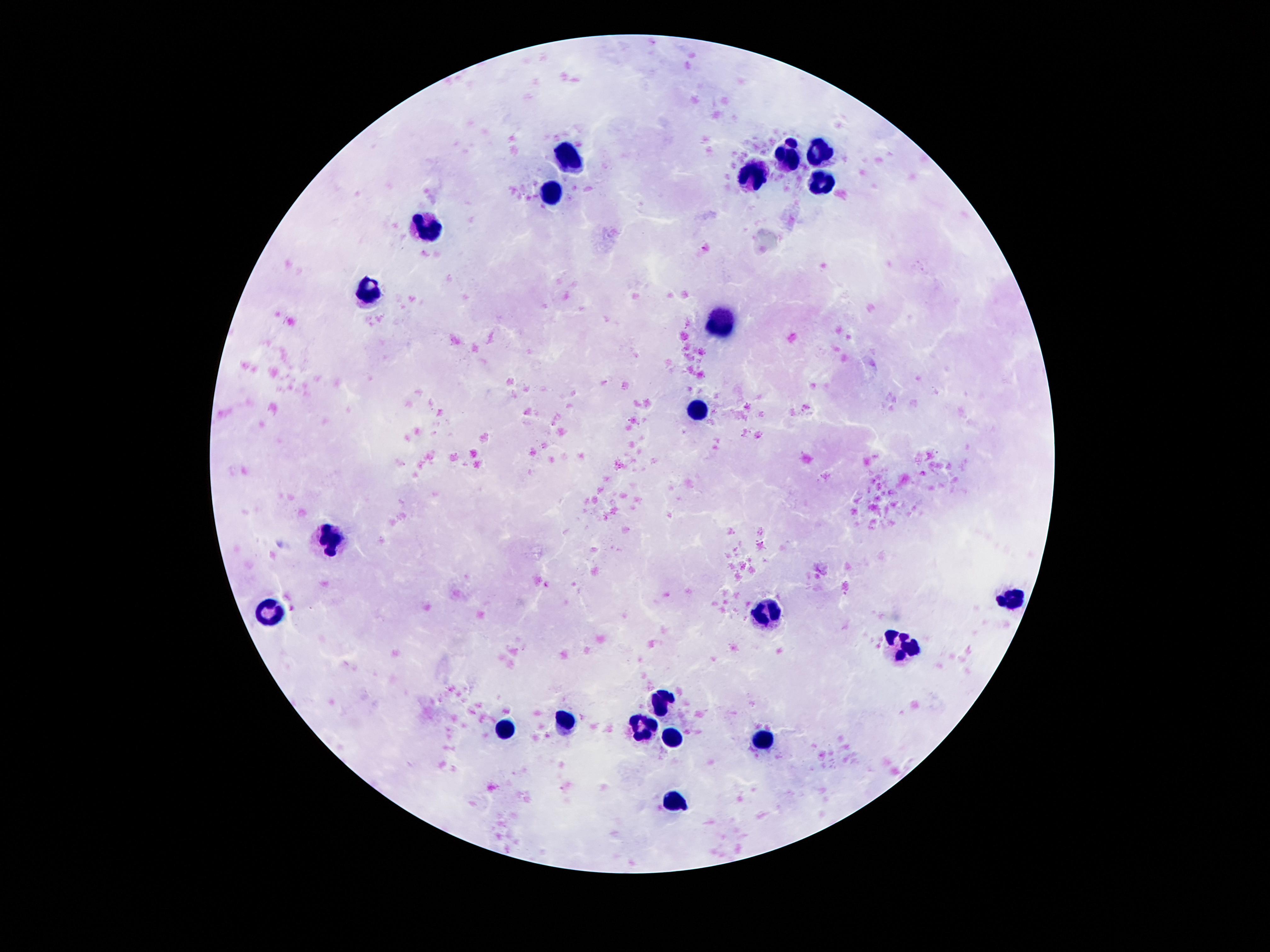
{
  "magnification": "100x",
  "preparation": "thick peripheral-blood smear",
  "image_size": "1270×952 pixels",
  "stain": "Giemsa",
  "patient_malaria_status": "negative",
  "field_of_view": "single",
  "leukocyte_locations": "approximate object centers, in pixels from the top-left corner: (x=823, y=153), (x=571, y=158), (x=791, y=158), (x=754, y=176), (x=821, y=185), (x=552, y=192), (x=431, y=228), (x=368, y=288), (x=723, y=320), (x=693, y=409), (x=330, y=537), (x=1014, y=598), (x=273, y=612), (x=767, y=615), (x=900, y=647), (x=661, y=701), (x=566, y=719), (x=645, y=727), (x=502, y=731), (x=670, y=738), (x=764, y=741), (x=670, y=800)",
  "capture": "smartphone camera through the microscope eyepiece"
}